Assess for Plasmodium parasites.
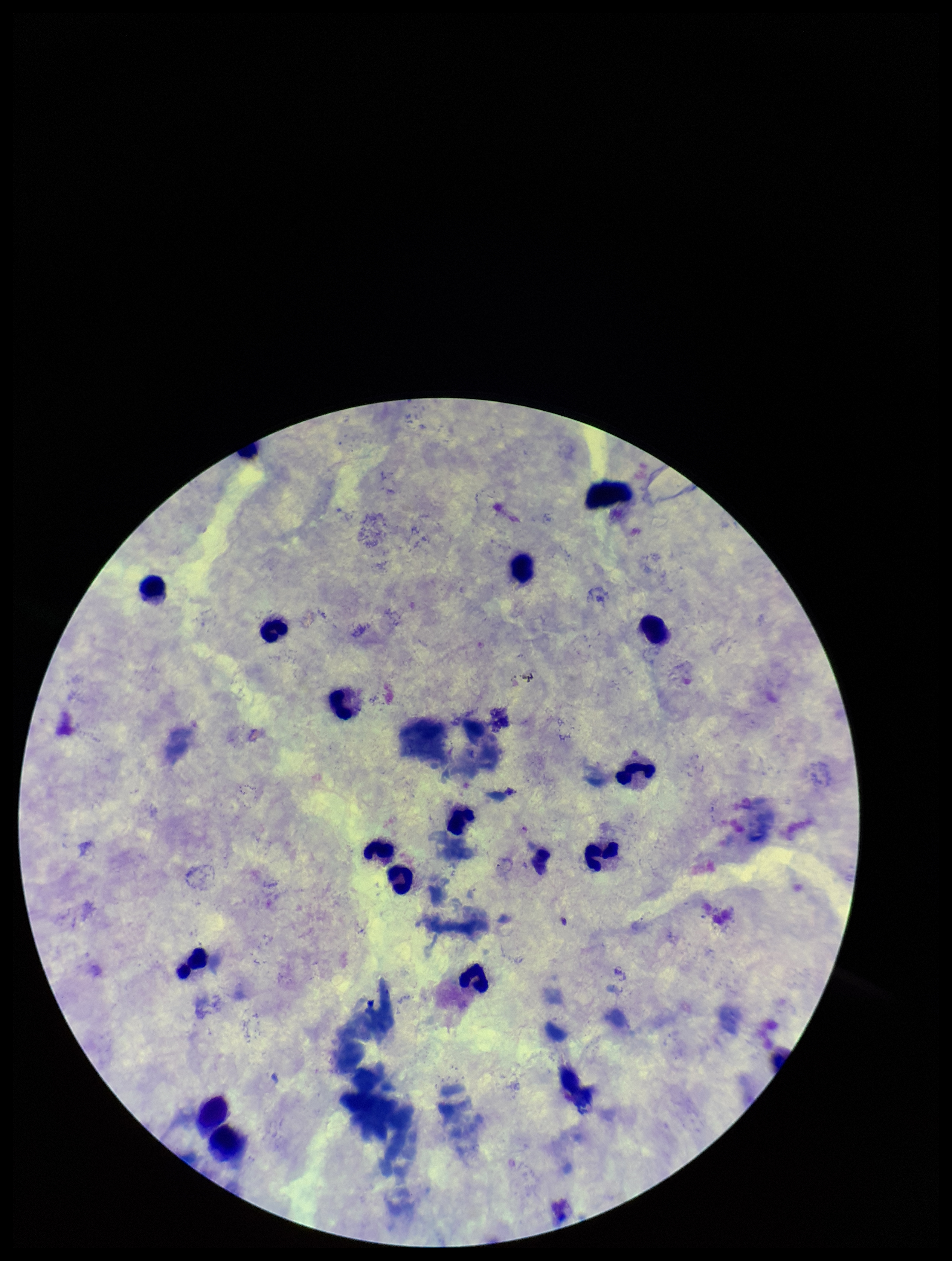
None identified.

Summary:
  - Stain: Giemsa
  - Field of view: one from this slide
  - Capture: smartphone photograph through the microscope eyepiece
  - Patient malaria status: negative
  - Preparation: thick smear
  - Image size: 952×1261 pixels
  - Leukocyte count: 13
  - Parasite count: 0